Outline each Plasmodium malariae-infected red blood cell.
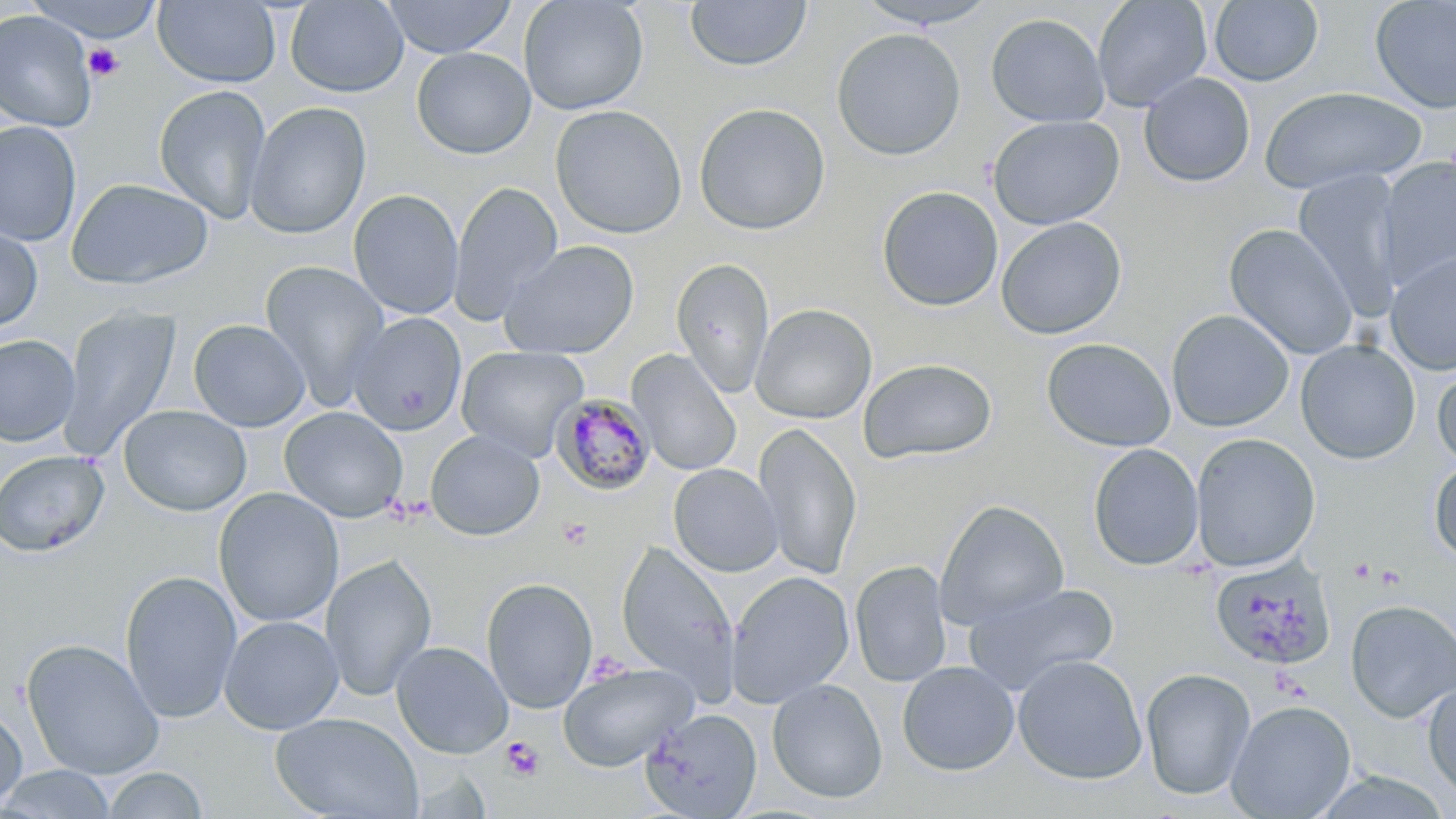

Approximate bounding boxes as (x1, y1, x2, y2) in pixels.
Plasmodium malariae-infected red blood cells: (552, 392, 656, 495).

slide_level_diagnosis: Plasmodium malariae
field_of_view: one of a larger specimen
preparation: thin blood film
stain: May-Grünwald-Giemsa
modality: optical microscopy
platelet_locations: 'approximate bounding boxes as (x1, y1, x2, y2) in pixels: (83, 43, 126, 81), (557, 518, 593, 550), (1349, 557, 1375, 583), (1374, 565, 1406, 591), (501, 737, 544, 781)'
magnification: 1000x
image_size: 1456×819 pixels
uninfected_red_blood_cell_locations: 'approximate bounding boxes as (x1, y1, x2, y2) in pixels: (285, 0, 409, 97), (383, 0, 516, 59), (518, 0, 649, 116), (685, 0, 812, 72), (853, 0, 1002, 29), (1092, 0, 1212, 111), (1209, 0, 1323, 86), (1370, 0, 1456, 113), (27, 1, 166, 45), (153, 1, 282, 87), (0, 10, 97, 132), (986, 13, 1110, 128), (831, 28, 966, 161), (411, 47, 536, 159), (1138, 72, 1255, 188), (153, 84, 272, 225), (1259, 86, 1427, 195), (245, 102, 371, 239), (693, 103, 831, 235), (550, 105, 687, 239), (988, 115, 1125, 230), (0, 121, 81, 247), (1378, 157, 1456, 286), (1293, 170, 1403, 319), (66, 177, 214, 290), (448, 180, 563, 324), (876, 185, 1004, 311), (348, 189, 464, 320), (995, 216, 1127, 339), (0, 221, 43, 334), (1224, 223, 1360, 359), (499, 240, 638, 360), (1385, 250, 1456, 376), (671, 257, 775, 398), (259, 260, 390, 408), (750, 303, 877, 424), (58, 305, 181, 461), (1166, 309, 1295, 432), (348, 312, 466, 436), (188, 319, 310, 431), (345, 328, 580, 442), (0, 334, 80, 447), (1041, 337, 1176, 451), (1295, 339, 1420, 464), (456, 346, 588, 461), (627, 350, 742, 476), (857, 357, 998, 464), (1433, 363, 1456, 474), (118, 404, 251, 517), (279, 406, 408, 523), (754, 422, 862, 580), (425, 430, 545, 541), (1190, 433, 1321, 572), (1087, 444, 1203, 571), (0, 450, 109, 557), (1429, 458, 1456, 563), (668, 464, 783, 577), (213, 487, 344, 628), (935, 499, 1069, 630), (617, 541, 739, 697), (320, 553, 437, 701), (1209, 559, 1335, 672), (850, 560, 952, 687), (119, 570, 243, 724), (726, 571, 854, 708), (481, 577, 597, 713), (964, 581, 1120, 696), (1344, 600, 1456, 723), (219, 615, 343, 734), (21, 638, 165, 780), (391, 641, 513, 759), (1012, 654, 1147, 784), (897, 661, 1020, 776), (558, 662, 698, 771), (1140, 668, 1256, 801), (767, 678, 887, 803), (1422, 680, 1456, 803), (1226, 699, 1356, 818), (642, 702, 888, 810), (0, 703, 27, 814), (641, 708, 762, 818), (270, 712, 423, 819), (0, 765, 117, 818), (100, 767, 209, 819)'